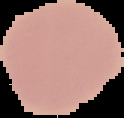 Result: no Plasmodium parasites detected. From a thin blood smear. Image is 124×118 pixels. The area outside the segmented cell region is set to black.